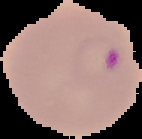

image_type: cell region segmented out of the field of view; surrounding area masked to black
preparation: thin blood film
malaria_status: parasitized
image_size: 142×139 pixels